Locate platelets.
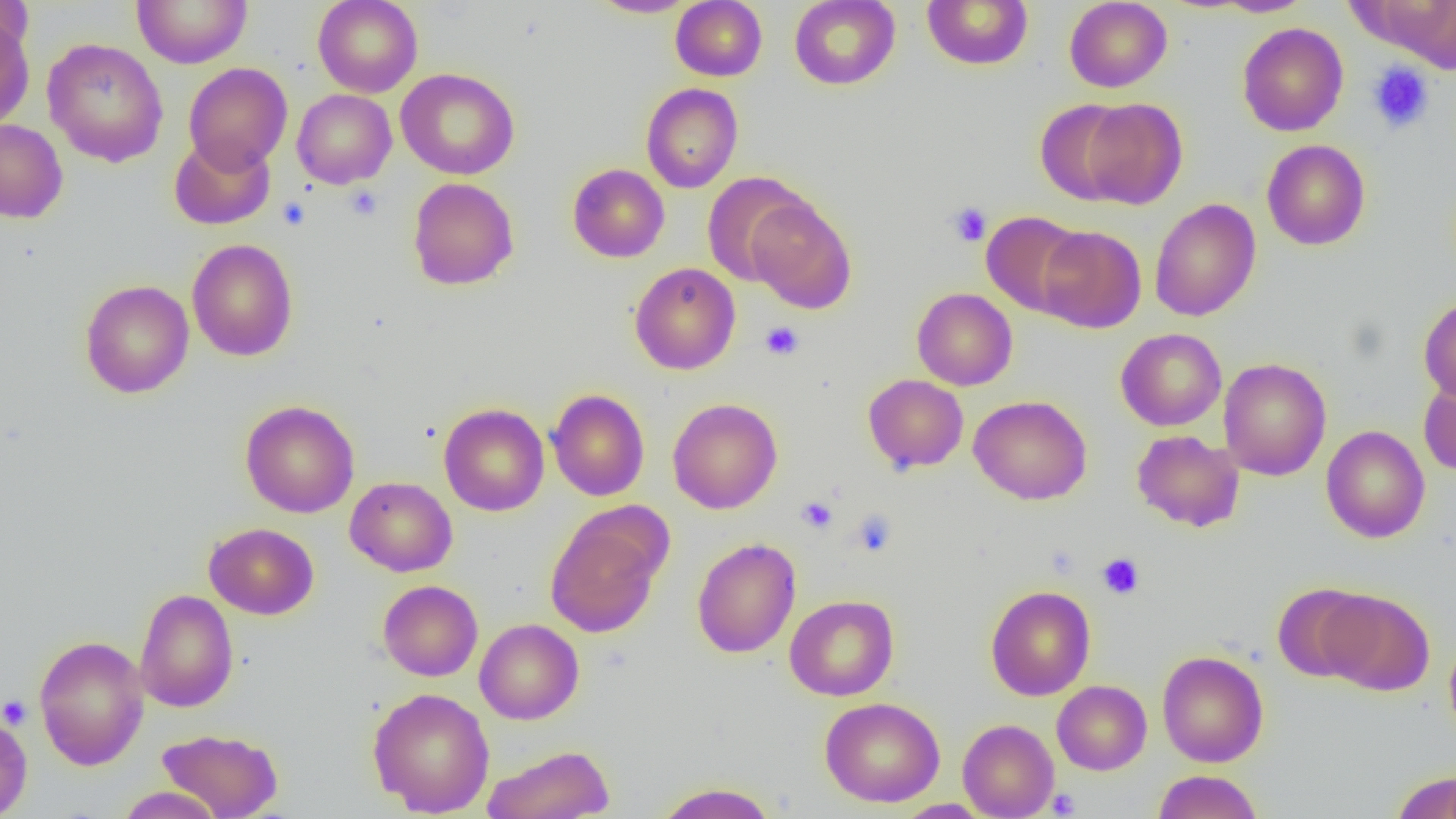

Approximate bounding boxes as [x1, y1, x2, y2] in pixels.
Platelets (subset): [1367, 60, 1435, 134], [344, 186, 383, 221], [946, 202, 992, 247], [760, 321, 804, 360], [797, 495, 838, 534], [849, 509, 898, 558], [1097, 553, 1145, 598], [0, 695, 32, 729], [1047, 787, 1081, 817].

{
  "slide_level_diagnosis": "negative for blood parasites",
  "field_of_view": "one of a larger specimen",
  "image_size": "1456×819 pixels",
  "preparation": "thin blood smear",
  "modality": "optical microscopy",
  "uninfected_red_blood_cell_locations_subset": "approximate bounding boxes as [x1, y1, x2, y2] in pixels: [0, 0, 33, 60], [132, 0, 252, 68], [313, 0, 423, 98], [589, 0, 697, 18], [670, 0, 767, 81], [789, 0, 901, 90], [922, 0, 1033, 70], [1064, 0, 1172, 92], [1211, 0, 1316, 17], [1362, 1, 1456, 73], [0, 15, 35, 131], [43, 38, 168, 167], [183, 62, 292, 172], [396, 68, 520, 180], [641, 82, 743, 193], [292, 89, 397, 189], [1080, 98, 1187, 209], [1035, 99, 1135, 205], [0, 118, 68, 223], [168, 134, 276, 230], [1261, 139, 1370, 250], [567, 164, 670, 262], [702, 173, 812, 286], [407, 177, 519, 290], [745, 197, 857, 313], [1149, 198, 1261, 321], [982, 211, 1086, 316], [1036, 225, 1146, 333], [187, 238, 298, 361], [629, 263, 741, 375], [79, 279, 194, 398], [911, 288, 1018, 390], [1419, 296, 1456, 406], [1115, 328, 1227, 431], [1218, 357, 1332, 481], [1418, 372, 1456, 477], [862, 374, 969, 473], [547, 389, 650, 501], [968, 395, 1093, 505], [667, 397, 783, 514], [240, 400, 360, 518], [439, 403, 549, 516], [1320, 425, 1430, 543], [1131, 430, 1244, 532], [345, 476, 457, 576], [545, 513, 665, 638], [204, 522, 319, 620], [691, 537, 801, 658], [377, 580, 483, 681], [1272, 583, 1376, 683], [985, 585, 1095, 700], [134, 589, 238, 712], [1317, 589, 1435, 696], [784, 594, 899, 701], [474, 618, 584, 724], [33, 635, 149, 771], [1444, 636, 1456, 745], [1157, 650, 1269, 767], [1052, 680, 1152, 775], [368, 688, 495, 816], [820, 696, 945, 807], [0, 715, 32, 818], [958, 719, 1059, 819], [157, 728, 284, 819], [482, 744, 615, 819], [1153, 770, 1263, 819], [1390, 771, 1456, 819], [653, 782, 779, 819], [115, 786, 224, 818], [893, 799, 992, 818]",
  "magnification": "1000x"
}